Locate every Plasmodium falciparum-infected red blood cell.
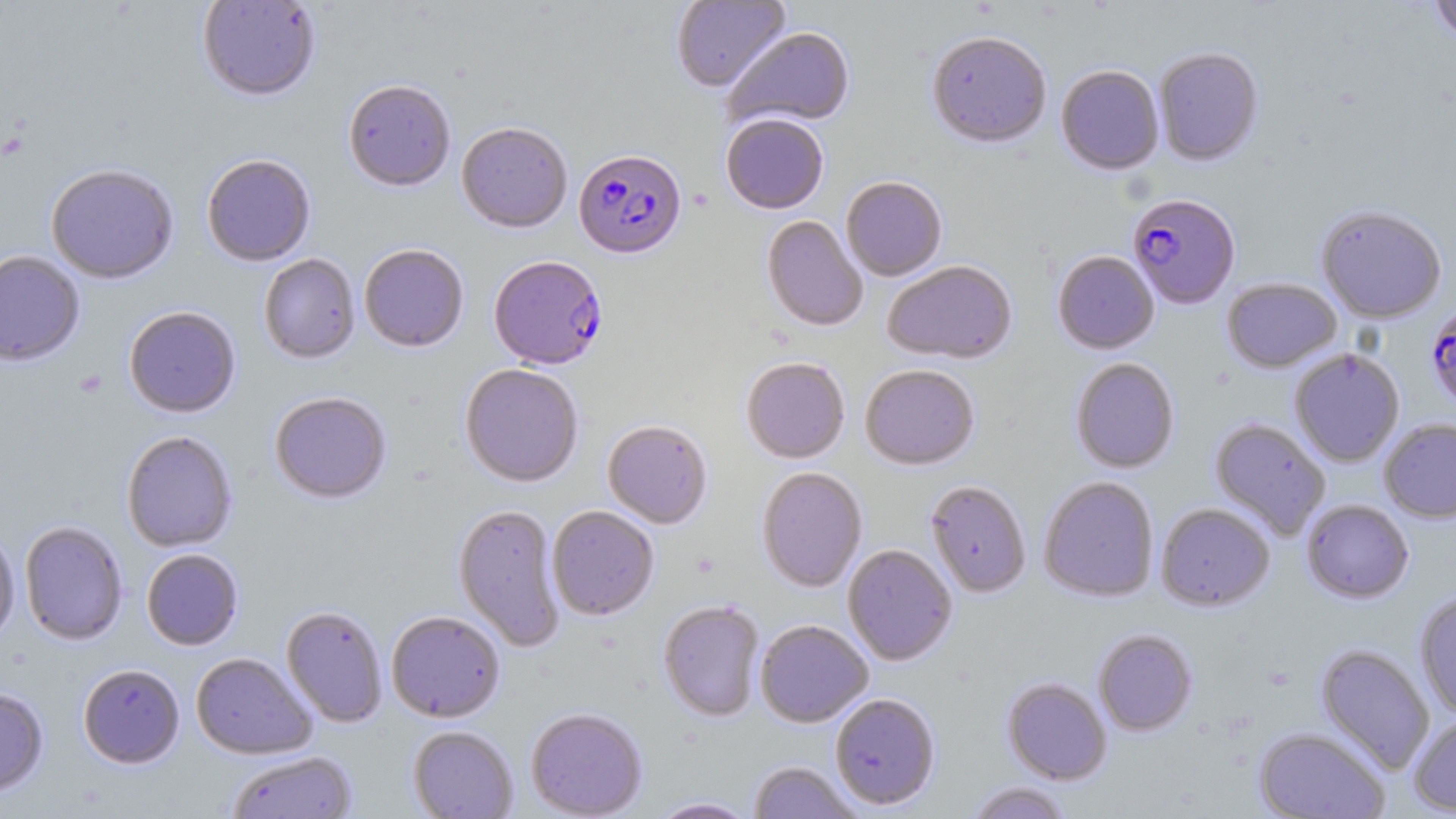

Approximate bounding boxes as [x1, y1, x2, y2] in pixels.
Plasmodium falciparum-infected red blood cells: [573, 152, 687, 262], [1127, 194, 1240, 311], [488, 257, 608, 372], [1425, 302, 1456, 414].

{
  "slide_level_diagnosis": "Plasmodium falciparum",
  "stain": "May-Grünwald-Giemsa",
  "preparation": "thin blood smear",
  "field_of_view": "one of a larger specimen",
  "uninfected_red_blood_cell_locations": "approximate bounding boxes as [x1, y1, x2, y2] in pixels: [197, 0, 321, 104], [671, 0, 791, 94], [1429, 0, 1456, 44], [725, 28, 855, 130], [926, 34, 1051, 151], [1154, 49, 1263, 167], [1056, 67, 1164, 177], [343, 82, 455, 194], [720, 116, 829, 216], [456, 125, 572, 235], [202, 156, 316, 268], [46, 166, 179, 285], [841, 178, 947, 282], [1316, 206, 1447, 324], [761, 216, 867, 333], [359, 246, 469, 354], [0, 251, 84, 367], [1052, 252, 1159, 355], [259, 255, 360, 365], [882, 262, 1017, 365], [1222, 278, 1341, 373], [124, 308, 241, 419], [1289, 349, 1405, 467], [741, 358, 850, 465], [1070, 359, 1179, 474], [460, 365, 583, 489], [860, 365, 979, 471], [269, 393, 392, 505], [1209, 418, 1331, 541], [1379, 419, 1456, 523], [602, 421, 712, 530], [121, 432, 238, 552], [757, 468, 867, 593], [1038, 477, 1159, 603], [925, 480, 1031, 598], [1301, 499, 1414, 604], [1156, 503, 1275, 612], [452, 504, 566, 652], [547, 506, 659, 621], [19, 522, 127, 646], [0, 528, 20, 648], [843, 545, 957, 666], [141, 550, 243, 651], [1414, 592, 1456, 720], [658, 601, 765, 722], [281, 606, 388, 727], [386, 612, 505, 724], [756, 620, 873, 728], [1093, 629, 1197, 736], [1315, 644, 1435, 775], [191, 653, 316, 760], [79, 665, 185, 769], [1001, 677, 1112, 785], [0, 687, 49, 799], [830, 694, 940, 810], [525, 708, 648, 819], [1408, 713, 1456, 815], [407, 726, 518, 819], [1253, 728, 1390, 818], [226, 751, 357, 819], [748, 761, 863, 819], [964, 781, 1074, 819], [648, 797, 759, 818]",
  "modality": "light microscopy",
  "image_size": "1456×819 pixels",
  "magnification": "1000x"
}